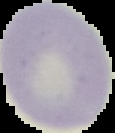
malaria_status: uninfected
image_type: segmented cell region with the area outside set to black
preparation: thin blood smear
image_size: 115×133 pixels